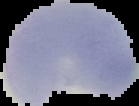

Summary:
  - Malaria status: parasitized
  - Preparation: thin blood film
  - Image size: 139×106 pixels
  - Image type: segmented cell region with the area outside set to black